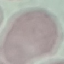

Malaria status: uninfected. Acquired by smartphone through the microscope eyepiece. Thin blood smear. Automatically extracted cell patch, resized to 64 × 64 pixels. Giemsa stain.